Outline each uninfected red blood cell.
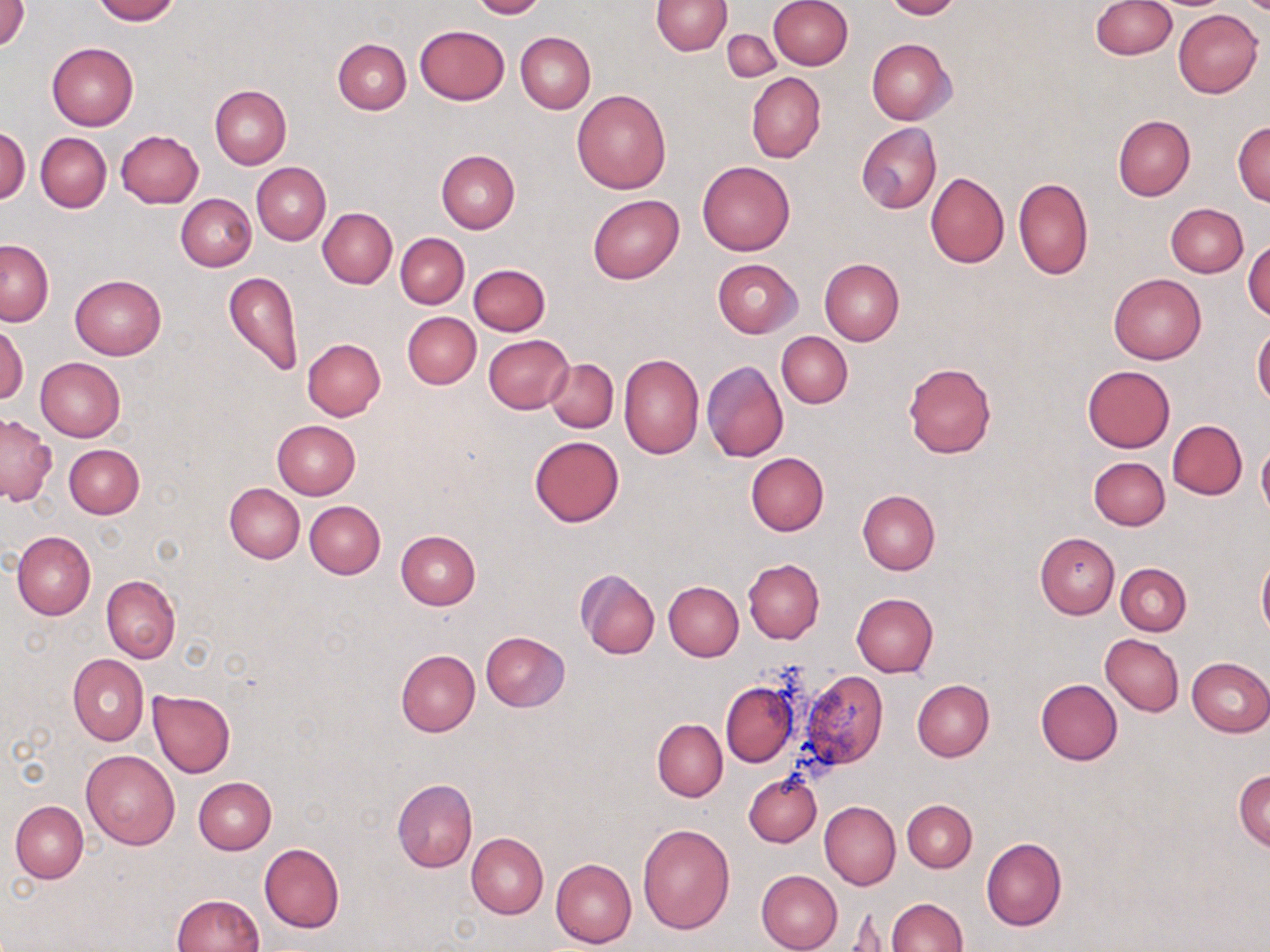
Approximate bounding boxes as (x1,y1)-(x2,y2) corner pairs in pixels.
Uninfected red blood cells: (1,0)-(29,50), (91,0)-(180,23), (470,0)-(548,19), (652,0)-(731,55), (768,0)-(852,70), (884,0)-(963,20), (1089,0)-(1175,58), (1173,8)-(1263,97), (415,24)-(509,104), (721,30)-(779,83), (515,32)-(595,114), (333,38)-(411,114), (867,38)-(956,125), (47,43)-(138,130), (746,73)-(826,162), (209,84)-(291,169), (572,89)-(672,194), (1113,115)-(1195,200), (1232,120)-(1270,207), (856,122)-(941,214), (1,128)-(29,203), (116,130)-(203,208), (35,132)-(112,212), (436,149)-(520,233), (698,160)-(795,256), (252,162)-(330,245), (925,172)-(1009,268), (1013,176)-(1093,280), (177,194)-(256,271), (587,194)-(683,283), (1166,204)-(1248,278), (317,208)-(397,288), (395,233)-(469,309), (1244,238)-(1270,322), (1,240)-(53,325), (819,258)-(904,345), (713,259)-(801,337), (469,264)-(550,335), (224,271)-(302,376), (1109,273)-(1206,364), (69,274)-(165,360), (401,312)-(480,389), (0,324)-(28,405), (1252,327)-(1270,407), (776,332)-(853,408), (483,335)-(573,414), (302,338)-(386,420), (618,353)-(704,459), (35,357)-(125,442), (546,357)-(618,432), (701,360)-(788,462), (903,363)-(996,457), (1082,365)-(1176,452), (0,413)-(56,505), (272,419)-(360,499), (1168,420)-(1247,499), (528,434)-(624,528), (1257,442)-(1270,521), (64,444)-(144,519), (746,452)-(829,536), (1089,456)-(1170,530), (224,482)-(304,563), (857,489)-(940,575), (305,500)-(385,578), (12,530)-(95,621), (395,530)-(481,609), (1034,532)-(1120,619), (1257,554)-(1270,642), (743,558)-(824,643), (1116,562)-(1191,635), (575,569)-(660,660), (101,575)-(180,662), (664,581)-(743,661), (851,592)-(937,678), (480,631)-(570,711), (1100,634)-(1184,716), (396,650)-(480,736), (68,654)-(148,745), (1185,657)-(1270,737), (801,670)-(887,767), (1035,679)-(1123,765), (912,680)-(994,761), (720,681)-(798,767), (148,689)-(235,778), (653,717)-(727,802), (82,749)-(180,849), (1234,769)-(1270,852), (743,772)-(822,847), (193,777)-(276,854), (391,778)-(477,873), (903,799)-(977,872), (11,800)-(88,883), (820,800)-(900,890), (637,823)-(735,934), (466,833)-(548,919), (981,838)-(1067,931), (259,843)-(345,933), (550,858)-(636,950), (755,870)-(843,952), (171,893)-(264,952), (885,897)-(967,952), (843,911)-(893,951).

Summary:
  - Slide-level diagnosis: negative for blood parasites
  - Stain: May-Grünwald-Giemsa
  - Modality: optical microscopy
  - Preparation: thin blood smear
  - Image size: 1270×952 pixels
  - Magnification: 1000x
  - Field of view: single